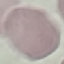
Summary:
  - Malaria status: uninfected
  - Stain: Giemsa
  - Capture: smartphone through the microscope eyepiece
  - Preparation: thin blood film
  - Image type: automatically extracted cell patch, resized to 64 × 64 pixels